Classify this cell by malaria status.
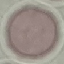

Uninfected.

capture = smartphone camera at the microscope eyepiece
image type = cell patch, automatically extracted from a larger field of view and resized to 64 × 64 pixels
stain = Giemsa
preparation = thin blood smear